Describe the morphology of the red blood cells.
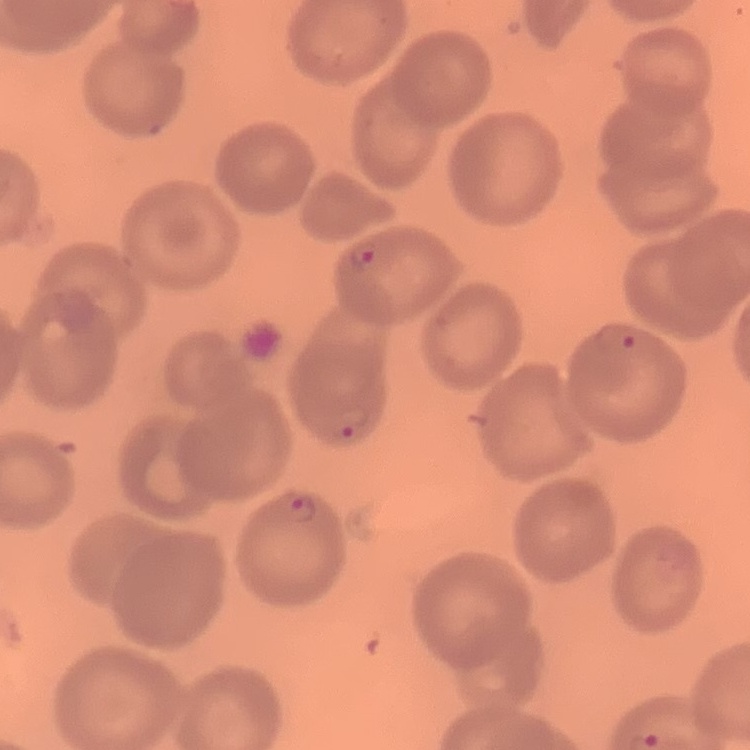

No rouleaux formation.

image_type: one tile cut from a larger photomicrograph
stain: Field's or Giemsa
preparation: thin blood film